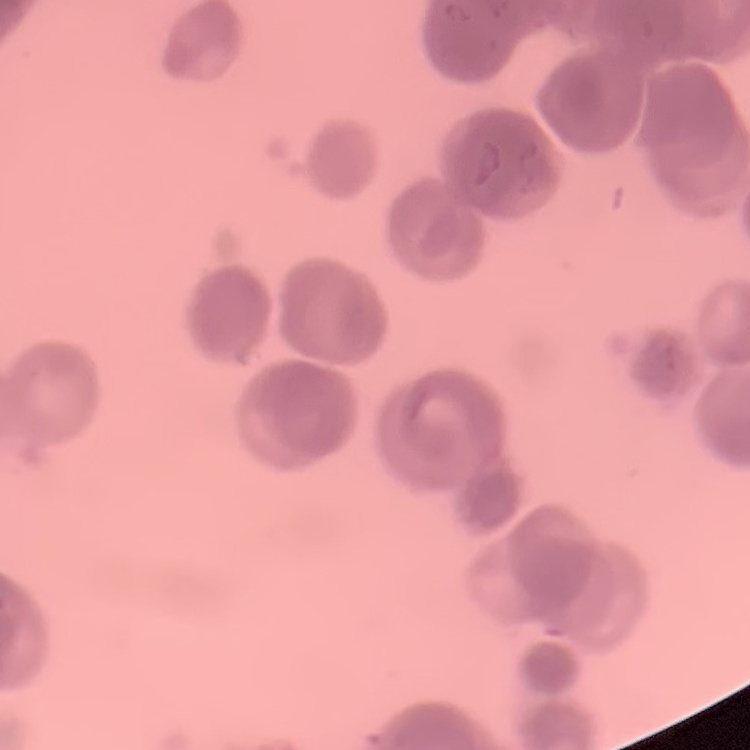 The red blood cells show rouleaux formation. Field's or Giemsa stain. One tile cut from a larger photomicrograph. Thin blood smear.